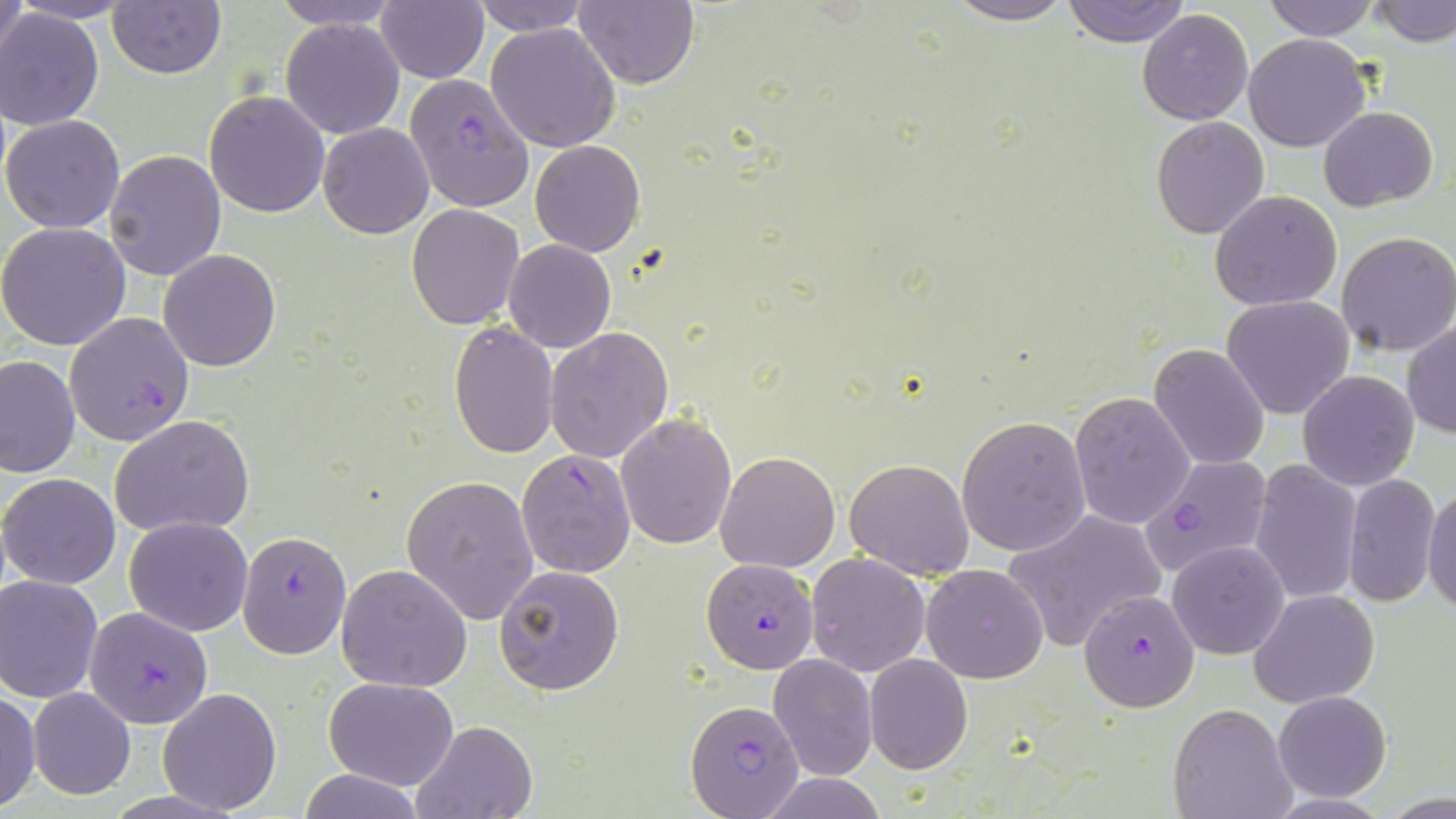
Approximate bounding boxes as named x1/y1/x2/y2 corners in pixels. Plasmodium falciparum-infected red blood cell locations: (x1=403, y1=72, x2=536, y2=214), (x1=64, y1=311, x2=194, y2=446), (x1=516, y1=448, x2=636, y2=577), (x1=1140, y1=455, x2=1272, y2=578), (x1=239, y1=531, x2=351, y2=657), (x1=699, y1=557, x2=817, y2=677), (x1=1080, y1=589, x2=1199, y2=711), (x1=84, y1=608, x2=212, y2=730), (x1=686, y1=699, x2=805, y2=816). Uninfected red blood cell locations: (x1=1, y1=0, x2=30, y2=81), (x1=268, y1=0, x2=405, y2=31), (x1=375, y1=0, x2=489, y2=84), (x1=473, y1=0, x2=589, y2=36), (x1=942, y1=0, x2=1079, y2=25), (x1=1060, y1=0, x2=1191, y2=46), (x1=1262, y1=0, x2=1381, y2=41), (x1=1371, y1=0, x2=1456, y2=48), (x1=10, y1=1, x2=139, y2=23), (x1=573, y1=1, x2=699, y2=89), (x1=107, y1=2, x2=226, y2=79), (x1=0, y1=8, x2=104, y2=130), (x1=1137, y1=10, x2=1254, y2=125), (x1=281, y1=18, x2=404, y2=139), (x1=485, y1=23, x2=621, y2=151), (x1=1243, y1=34, x2=1370, y2=152), (x1=204, y1=91, x2=330, y2=217), (x1=1319, y1=105, x2=1440, y2=211), (x1=1, y1=114, x2=127, y2=235), (x1=1150, y1=117, x2=1270, y2=238), (x1=318, y1=122, x2=433, y2=239), (x1=530, y1=139, x2=645, y2=256), (x1=104, y1=149, x2=228, y2=281), (x1=1211, y1=190, x2=1342, y2=312), (x1=407, y1=203, x2=524, y2=329), (x1=0, y1=223, x2=132, y2=350), (x1=1335, y1=232, x2=1456, y2=356), (x1=503, y1=240, x2=615, y2=352), (x1=157, y1=249, x2=281, y2=371), (x1=1221, y1=295, x2=1354, y2=420), (x1=1403, y1=319, x2=1456, y2=439), (x1=448, y1=322, x2=558, y2=457), (x1=546, y1=328, x2=673, y2=463), (x1=1149, y1=343, x2=1271, y2=469), (x1=0, y1=355, x2=79, y2=479), (x1=1297, y1=370, x2=1419, y2=491), (x1=1069, y1=391, x2=1196, y2=530), (x1=616, y1=413, x2=737, y2=550), (x1=109, y1=415, x2=256, y2=538), (x1=957, y1=416, x2=1091, y2=557), (x1=716, y1=452, x2=839, y2=572), (x1=843, y1=456, x2=975, y2=581), (x1=1249, y1=460, x2=1362, y2=604), (x1=2, y1=472, x2=121, y2=589), (x1=1344, y1=472, x2=1440, y2=609), (x1=401, y1=475, x2=540, y2=622), (x1=1424, y1=475, x2=1456, y2=617), (x1=1004, y1=511, x2=1165, y2=653), (x1=123, y1=517, x2=253, y2=636), (x1=1168, y1=541, x2=1288, y2=659), (x1=805, y1=552, x2=932, y2=676), (x1=922, y1=563, x2=1048, y2=684), (x1=336, y1=564, x2=472, y2=692), (x1=495, y1=564, x2=624, y2=695), (x1=0, y1=575, x2=103, y2=703), (x1=1250, y1=589, x2=1380, y2=707), (x1=767, y1=653, x2=878, y2=781), (x1=864, y1=655, x2=973, y2=773), (x1=323, y1=677, x2=461, y2=789), (x1=26, y1=686, x2=137, y2=799), (x1=158, y1=686, x2=281, y2=814), (x1=0, y1=687, x2=40, y2=812), (x1=1273, y1=691, x2=1392, y2=802), (x1=1168, y1=704, x2=1297, y2=819), (x1=411, y1=719, x2=538, y2=819), (x1=297, y1=769, x2=426, y2=819), (x1=762, y1=775, x2=888, y2=817). Slide-level diagnosis: Plasmodium falciparum. Light microscopy. Thin blood smear. Image is 1456×819 pixels. Captured at 1000x magnification. May-Grünwald-Giemsa-stained preparation. Single field of view.